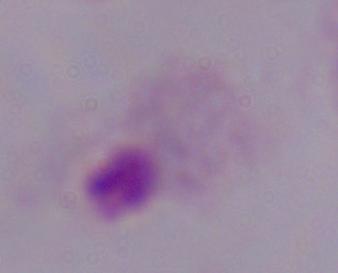

Summary:
  - Magnification: 1000x
  - Modality: micrograph
  - Identification: trichomonad